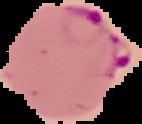
result: malaria parasites detected
image_size: 142×124 pixels
image_type: cell region segmented out of the field of view; surrounding area masked to black
preparation: thin blood film